Report the malaria status of this cell.
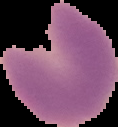

It is parasitized.

Summary:
  - Image size: 118×127 pixels
  - Image type: segmented cell region on a black background
  - Preparation: thin blood film